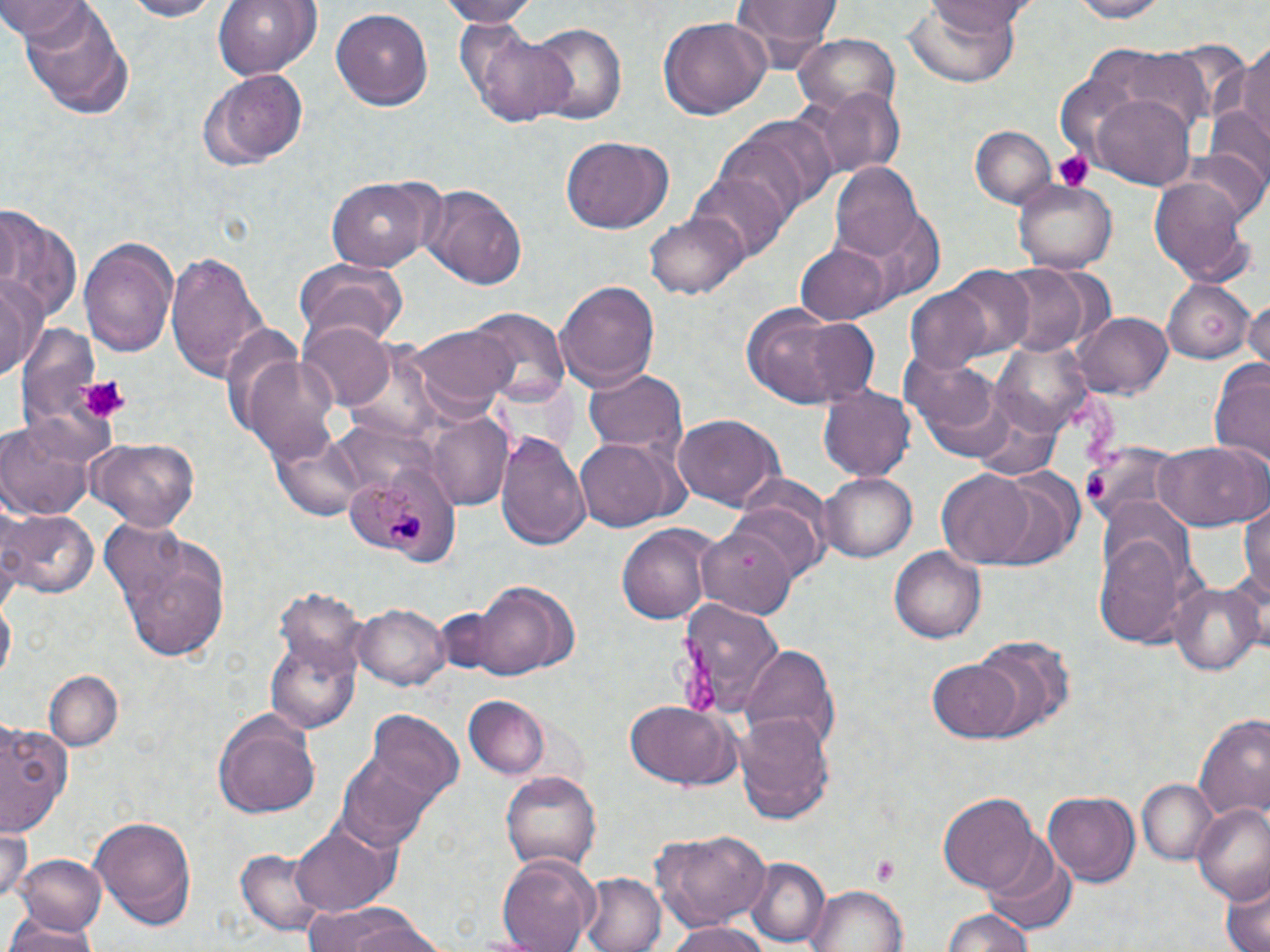 Approximate bounding boxes as (x1,y1)-(x2,y2) corner pairs in pixels. Uninfected red blood cell locations: (0,0)-(97,46), (119,0)-(220,20), (213,0)-(322,78), (436,0)-(539,25), (924,0)-(1033,34), (1067,0)-(1171,22), (729,1)-(844,55), (902,2)-(1023,88), (15,4)-(133,114), (330,7)-(433,110), (659,18)-(771,122), (527,21)-(628,129), (462,29)-(577,126), (793,36)-(900,120), (1232,40)-(1270,151), (1087,49)-(1213,163), (200,68)-(309,169), (804,88)-(902,182), (1090,96)-(1195,187), (719,113)-(835,221), (970,126)-(1054,207), (560,136)-(674,234), (1182,148)-(1269,227), (832,164)-(926,263), (692,171)-(788,264), (326,176)-(436,273), (1150,176)-(1253,282), (1014,181)-(1117,271), (418,184)-(527,290), (0,207)-(82,323), (646,209)-(747,299), (79,235)-(179,355), (795,244)-(890,323), (166,249)-(267,380), (295,259)-(411,348), (993,264)-(1093,357), (946,266)-(1034,357), (1,276)-(45,381), (556,277)-(660,386), (1162,277)-(1256,364), (905,286)-(994,374), (1243,299)-(1270,368), (741,303)-(876,410), (467,308)-(569,407), (1076,312)-(1171,400), (298,318)-(397,409), (15,319)-(113,449), (409,326)-(514,415), (993,338)-(1094,439), (903,349)-(1012,458), (240,353)-(345,464), (1207,358)-(1270,469), (582,367)-(688,459), (818,385)-(916,481), (425,412)-(512,509), (675,415)-(784,509), (0,416)-(99,519), (495,432)-(590,548), (576,436)-(675,532), (86,437)-(200,530), (1085,441)-(1192,525), (1153,441)-(1268,533), (936,468)-(1040,567), (820,472)-(917,563), (731,493)-(828,582), (1241,497)-(1270,618), (0,508)-(96,600), (1093,518)-(1195,648), (105,521)-(232,663), (617,523)-(713,625), (698,528)-(799,621), (891,547)-(983,644), (463,580)-(578,676), (1170,580)-(1263,675), (273,586)-(370,675), (1,595)-(14,686), (677,597)-(783,716), (355,602)-(450,689), (266,636)-(361,732), (971,638)-(1071,741), (738,643)-(839,753), (930,659)-(1026,741), (45,668)-(122,751), (463,696)-(549,780), (622,701)-(740,790), (368,711)-(465,803), (735,711)-(835,820), (213,714)-(320,819), (1195,716)-(1270,825), (0,721)-(74,837), (338,740)-(448,850), (501,770)-(600,870), (1137,779)-(1219,865), (1042,790)-(1138,886), (938,792)-(1043,892), (1191,803)-(1270,904), (89,812)-(198,930), (290,821)-(398,918), (0,823)-(30,902), (653,827)-(770,932), (982,842)-(1077,935), (234,848)-(336,938), (494,850)-(601,952), (14,854)-(105,937), (745,857)-(829,948), (578,871)-(667,952), (1219,882)-(1269,952), (809,884)-(909,952), (305,903)-(439,952), (939,908)-(1040,952), (1,923)-(100,952), (669,924)-(770,952). Plasmodium malariae-infected red blood cell locations: (347,468)-(459,566). Platelet locations: (1052,150)-(1092,191), (78,374)-(130,422), (1087,475)-(1107,502), (873,855)-(900,889). Slide-level diagnosis: Plasmodium malariae. Optical microscopy. May-Grünwald-Giemsa-stained preparation. Image is 1270×952 pixels. Captured at 1000x magnification. One field of a larger specimen. Thin blood film.